Describe the morphology of the red blood cells.
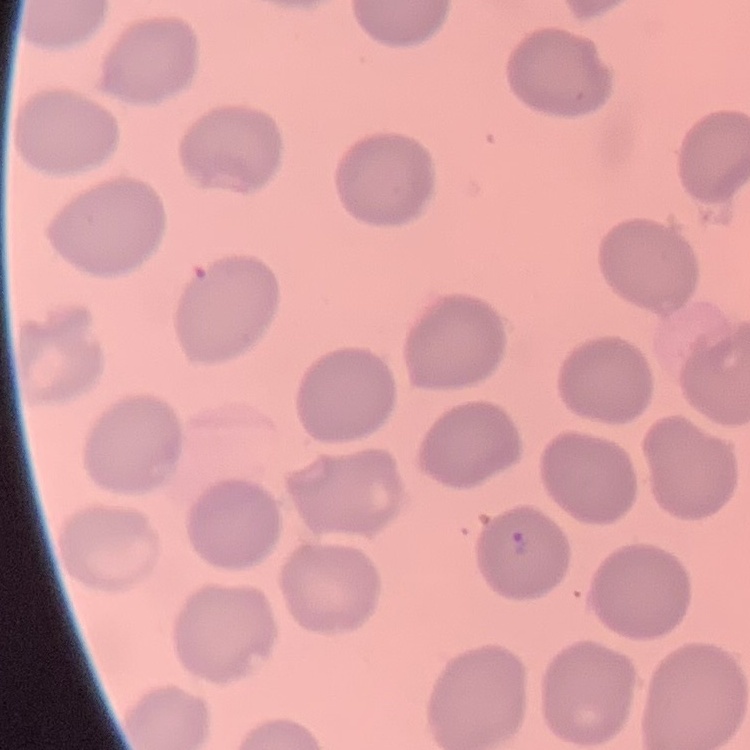
No rouleaux formation.

One tile cut from a larger photomicrograph. Field's or Giemsa stain. Thin blood smear.